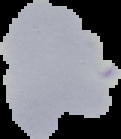

image_type: segmented cell region with the area outside set to black
image_size: 121×139 pixels
malaria_status: uninfected
preparation: thin blood film